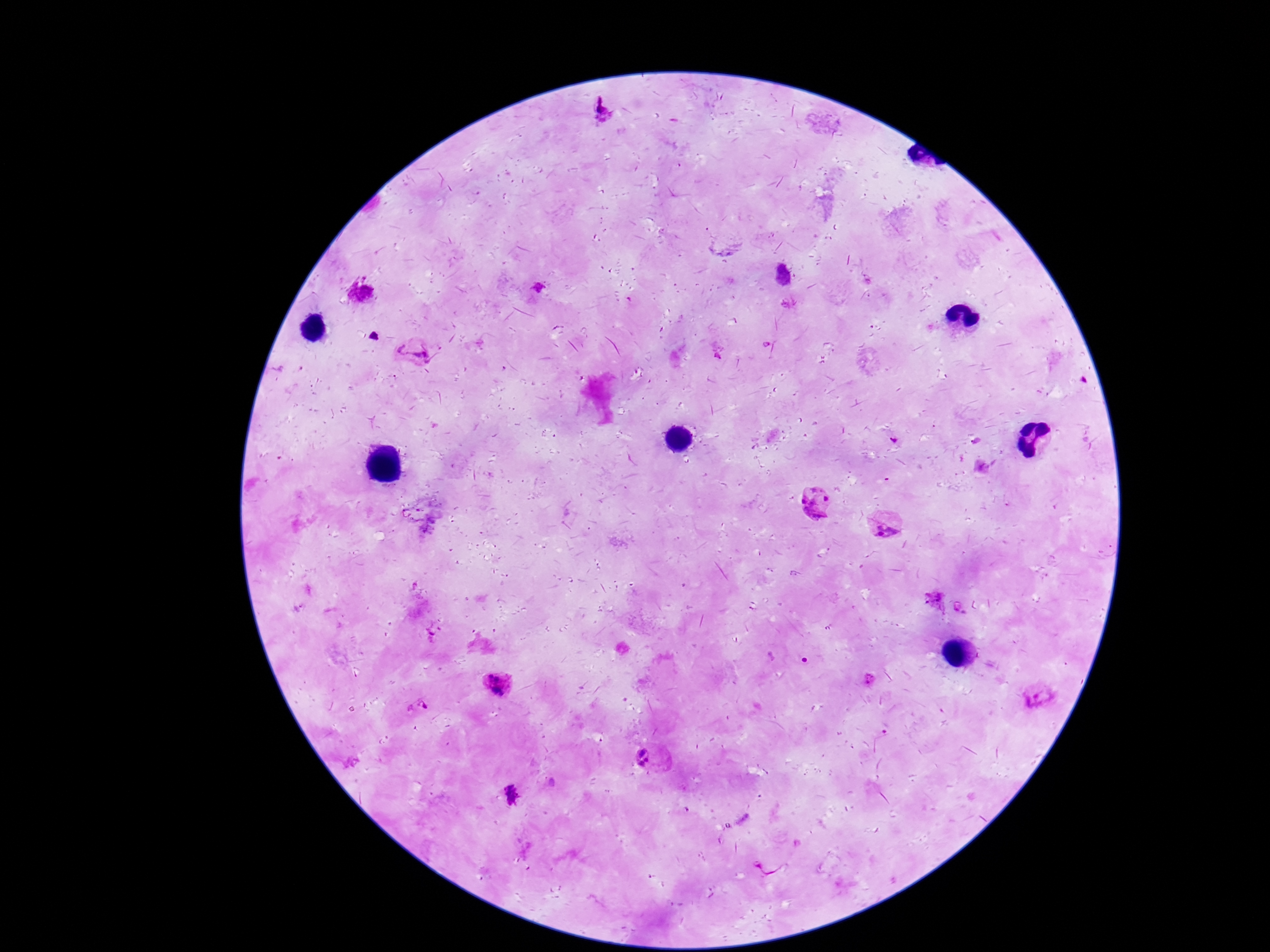
Approximate object centers, in pixels from the top-left corner. Plasmodium parasite locations: (x=602, y=109), (x=867, y=280), (x=539, y=287), (x=363, y=295), (x=788, y=304), (x=414, y=355), (x=893, y=441), (x=815, y=500), (x=887, y=526), (x=935, y=600), (x=432, y=633), (x=870, y=678), (x=497, y=683), (x=1037, y=696), (x=419, y=707), (x=651, y=759), (x=512, y=795). Image is 1270×952 pixels. Single field of view. Photographed through the microscope eyepiece with a smartphone camera. Thick blood smear. Patient malaria status: positive. 100x magnification. Giemsa-stained preparation.